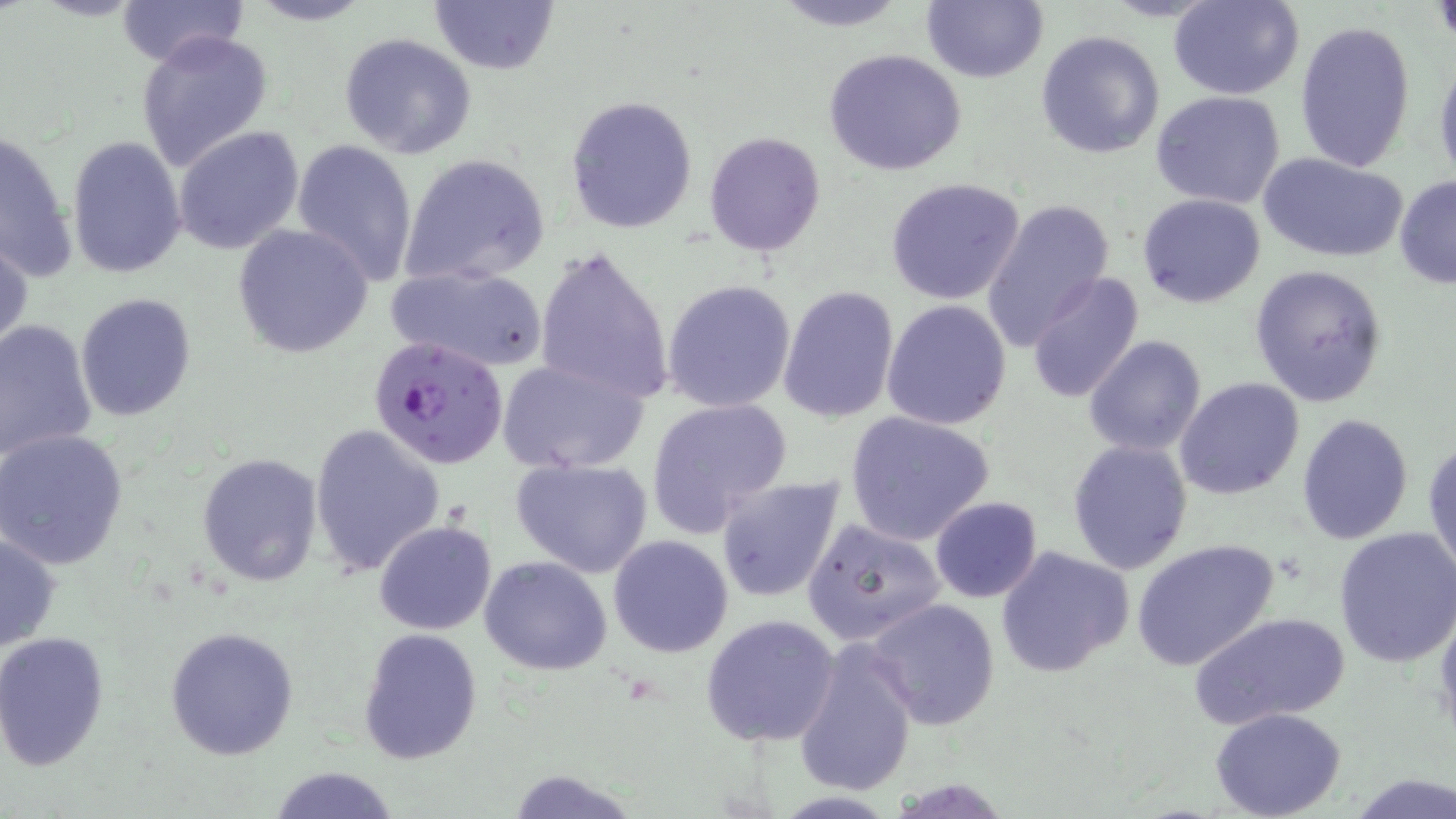 Approximate bounding boxes as (x1, y1, x2, y2) in pixels. Uninfected red blood cell locations: (114, 0, 249, 68), (244, 0, 375, 26), (429, 0, 561, 73), (765, 0, 915, 31), (922, 0, 1048, 84), (1169, 0, 1305, 100), (1295, 19, 1417, 173), (1035, 29, 1164, 158), (136, 31, 274, 172), (338, 33, 478, 158), (823, 49, 967, 177), (1434, 55, 1455, 190), (1152, 91, 1287, 208), (564, 95, 698, 235), (174, 126, 304, 254), (2, 128, 79, 284), (705, 132, 825, 255), (65, 136, 187, 279), (291, 138, 419, 287), (399, 152, 551, 288), (1259, 153, 1408, 264), (1394, 175, 1456, 289), (885, 177, 1026, 304), (1138, 193, 1266, 308), (981, 200, 1113, 345), (231, 223, 375, 357), (0, 228, 32, 359), (535, 243, 675, 409), (385, 264, 551, 373), (1248, 265, 1390, 408), (1026, 271, 1145, 406), (662, 280, 797, 414), (777, 285, 901, 424), (75, 294, 197, 423), (882, 299, 1012, 430), (0, 320, 98, 463), (1084, 335, 1207, 457), (496, 356, 648, 474), (1175, 376, 1305, 501), (646, 397, 792, 536), (844, 410, 996, 544), (1296, 412, 1415, 543), (309, 424, 444, 579), (0, 428, 129, 569), (1424, 434, 1456, 584), (1067, 440, 1193, 576), (195, 452, 324, 589), (509, 456, 654, 577), (716, 475, 847, 604), (930, 496, 1043, 603), (802, 516, 948, 648), (373, 520, 495, 636), (1333, 527, 1456, 668), (0, 531, 62, 654), (607, 534, 733, 658), (1130, 538, 1280, 671), (995, 547, 1135, 680), (481, 555, 612, 675), (866, 598, 999, 730), (1434, 604, 1456, 747), (1190, 612, 1348, 729), (700, 613, 841, 746), (165, 626, 298, 761), (358, 627, 484, 766), (0, 633, 109, 770), (793, 638, 918, 798), (1210, 708, 1348, 819), (267, 764, 402, 819), (502, 768, 639, 818), (1349, 772, 1456, 818). Plasmodium falciparum-infected red blood cell locations: (371, 334, 508, 468). Slide-level diagnosis: Plasmodium falciparum. Thin blood film. Image is 1456×819 pixels. One field of a larger specimen. Captured at 1000x magnification. May-Grünwald-Giemsa-stained preparation. Light microscopy.